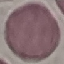
Result: no malaria parasites detected. Cell patch, automatically extracted from a larger field of view and resized to 64 × 64 pixels. Acquired by smartphone through the microscope eyepiece. Thin blood smear. Giemsa stain.